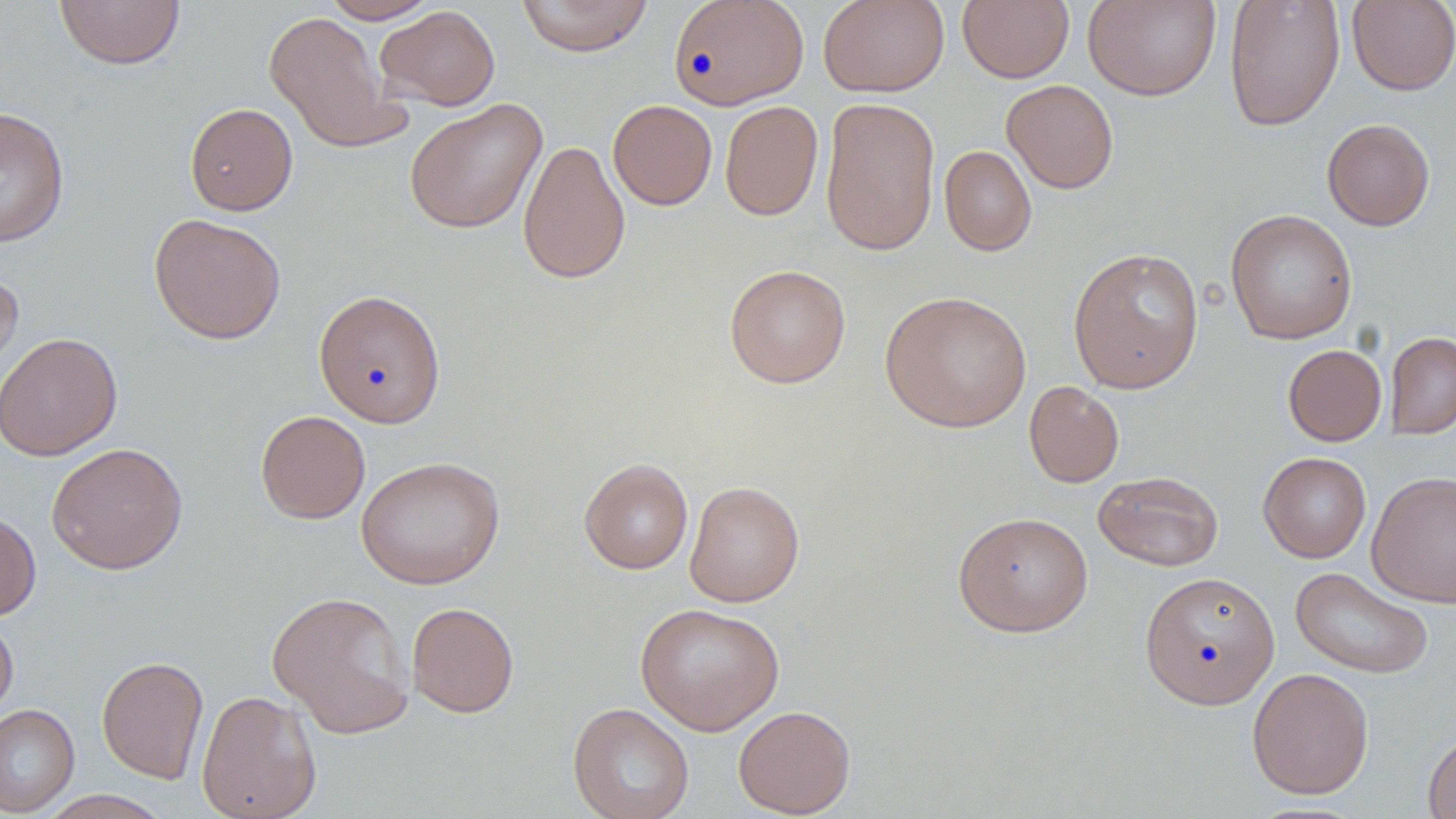

Summary:
  - Coordinate format: approximate bounding boxes as [x1, y1, x2, y2] in pixels
  - Uninfected red blood cell locations: [54, 0, 185, 70], [320, 0, 440, 23], [515, 0, 653, 57], [668, 0, 808, 109], [818, 0, 950, 97], [957, 0, 1074, 83], [1082, 0, 1221, 101], [1224, 0, 1345, 131], [1346, 1, 1456, 96], [374, 5, 501, 111], [263, 11, 411, 155], [1001, 79, 1118, 193], [820, 97, 941, 256], [405, 99, 547, 234], [608, 99, 718, 210], [719, 101, 823, 221], [184, 102, 298, 216], [0, 105, 70, 248], [1321, 118, 1435, 231], [517, 138, 630, 285], [939, 145, 1037, 256], [1225, 209, 1358, 345], [148, 213, 286, 344], [1067, 247, 1205, 394], [724, 263, 851, 388], [0, 264, 24, 384], [313, 289, 446, 428], [880, 290, 1032, 433], [1385, 331, 1456, 440], [0, 332, 123, 461], [1283, 344, 1386, 446], [1024, 381, 1124, 488], [255, 410, 370, 524], [46, 442, 188, 574], [1258, 452, 1371, 563], [356, 456, 505, 589], [579, 458, 693, 574], [1092, 470, 1224, 571], [1366, 470, 1456, 608], [685, 480, 805, 607], [0, 509, 41, 621], [953, 511, 1093, 637], [1290, 566, 1434, 679], [1139, 570, 1280, 710], [266, 590, 416, 739], [406, 602, 520, 718], [635, 602, 785, 735], [0, 610, 19, 724], [96, 655, 209, 784], [1247, 667, 1374, 799], [196, 689, 322, 819], [567, 702, 695, 819], [0, 703, 80, 816], [733, 705, 856, 818], [1423, 731, 1456, 819], [36, 790, 174, 819]
  - Slide-level diagnosis: negative for blood parasites
  - Field of view: one of a larger specimen
  - Preparation: thin blood film
  - Stain: May-Grünwald-Giemsa
  - Modality: light microscopy
  - Magnification: 1000x
  - Image size: 1456×819 pixels